Locate every blood parasite and identify its species.
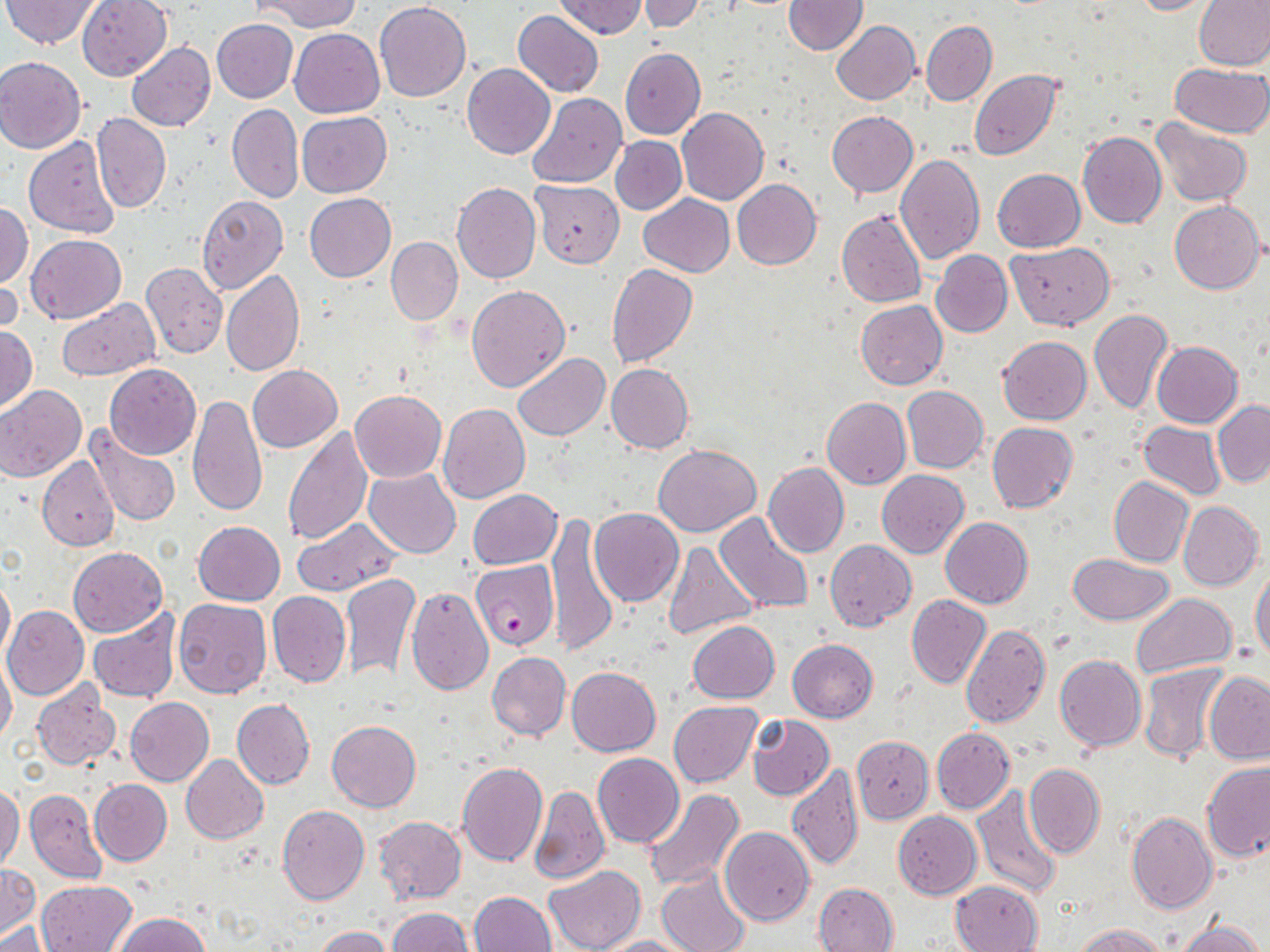

Approximate bounding boxes as (x1, y1, x2, y2) in pixels.
Plasmodium falciparum-infected red blood cells: (471, 559, 559, 650).
No Plasmodium ovale, Plasmodium malariae, Plasmodium vivax, Babesia divergens, or Trypanosoma brucei observed.

Summary:
  - Uninfected red blood cell locations: (2, 0, 102, 49), (77, 0, 172, 81), (255, 0, 363, 32), (555, 0, 647, 39), (636, 0, 710, 34), (783, 0, 867, 55), (1127, 0, 1216, 16), (1195, 0, 1270, 71), (374, 3, 471, 102), (513, 9, 604, 97), (212, 18, 298, 103), (832, 20, 920, 104), (921, 21, 997, 107), (289, 28, 384, 118), (127, 42, 215, 132), (620, 49, 705, 139), (0, 56, 86, 152), (462, 63, 555, 159), (1169, 63, 1268, 137), (970, 70, 1062, 160), (528, 92, 627, 187), (227, 103, 303, 203), (677, 106, 768, 205), (827, 111, 918, 198), (297, 112, 392, 197), (92, 113, 171, 213), (1152, 119, 1252, 206), (1078, 131, 1166, 229), (23, 135, 121, 238), (610, 135, 686, 214), (895, 153, 985, 264), (993, 168, 1084, 253), (731, 179, 821, 270), (531, 181, 625, 267), (452, 182, 541, 283), (305, 193, 396, 281), (639, 193, 734, 278), (197, 194, 288, 295), (1169, 200, 1265, 294), (0, 201, 33, 287), (836, 211, 927, 308), (25, 233, 126, 325), (385, 236, 463, 325), (1006, 243, 1115, 330), (932, 250, 1012, 337), (140, 262, 228, 359), (0, 263, 22, 339), (606, 264, 697, 368), (222, 270, 304, 376), (466, 285, 570, 391), (55, 297, 159, 380), (855, 300, 947, 390), (1088, 308, 1174, 416), (0, 324, 38, 413), (997, 336, 1092, 424), (1153, 341, 1242, 429), (513, 353, 609, 441), (606, 363, 694, 454), (104, 364, 201, 459), (247, 365, 342, 452), (1, 385, 86, 482), (902, 386, 988, 473), (351, 390, 446, 483), (189, 396, 266, 516), (823, 397, 911, 489), (1212, 402, 1270, 486), (438, 403, 529, 503), (1139, 421, 1228, 500), (986, 422, 1080, 513), (86, 424, 182, 527), (281, 426, 372, 545), (653, 444, 761, 535), (37, 457, 119, 551), (764, 463, 849, 559), (363, 468, 461, 557), (878, 469, 969, 558), (1109, 476, 1193, 567), (467, 489, 562, 569), (1177, 500, 1264, 591), (589, 508, 683, 607), (714, 511, 815, 614), (546, 514, 619, 653), (941, 517, 1033, 608), (292, 518, 401, 597), (193, 521, 285, 606), (825, 540, 916, 632), (661, 541, 758, 641), (68, 547, 167, 637), (1068, 553, 1175, 625), (1251, 568, 1270, 664), (0, 572, 14, 663), (340, 572, 421, 682), (407, 586, 493, 696), (267, 592, 350, 688), (1130, 593, 1237, 679), (906, 595, 990, 689), (173, 597, 271, 698), (3, 606, 89, 699), (87, 608, 181, 704), (688, 620, 780, 703), (962, 623, 1050, 728), (787, 638, 877, 722), (486, 651, 570, 740), (1055, 655, 1146, 752), (0, 656, 16, 745), (1139, 663, 1230, 764), (567, 666, 660, 756), (1204, 672, 1270, 764), (31, 682, 121, 771), (126, 697, 214, 786), (232, 698, 315, 789), (669, 701, 762, 788), (747, 714, 834, 801), (328, 720, 421, 813), (932, 728, 1014, 812), (852, 736, 933, 823), (593, 753, 684, 847), (181, 754, 269, 843), (457, 762, 548, 866), (1201, 762, 1270, 862), (787, 763, 864, 869), (1023, 764, 1104, 858), (90, 779, 172, 865), (1, 784, 22, 874), (528, 785, 609, 886), (971, 787, 1063, 899), (642, 788, 745, 890), (24, 789, 107, 884), (277, 804, 369, 905), (894, 811, 982, 899), (1126, 811, 1218, 913), (374, 817, 467, 904), (720, 828, 815, 926), (0, 862, 37, 938), (545, 865, 647, 952), (656, 870, 751, 952), (949, 879, 1043, 952), (37, 880, 138, 950), (813, 882, 899, 952), (470, 891, 556, 952), (386, 907, 475, 952), (115, 913, 211, 952), (0, 919, 55, 952), (1175, 919, 1262, 952), (1072, 923, 1169, 952), (312, 926, 394, 952), (602, 936, 690, 952)
  - Slide-level diagnosis: Plasmodium falciparum
  - Magnification: 1000x
  - Modality: optical microscopy
  - Stain: May-Grünwald-Giemsa
  - Field of view: single
  - Preparation: thin blood smear
  - Image size: 1270×952 pixels